Identify the parasite.
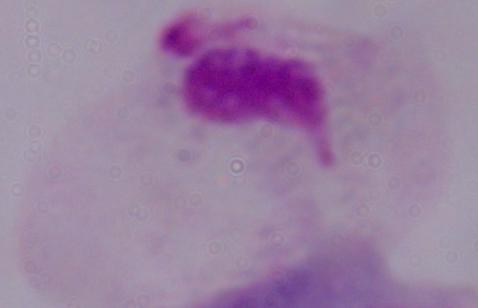
This is a trichomonad.

Micrograph. Captured at 1000x magnification.